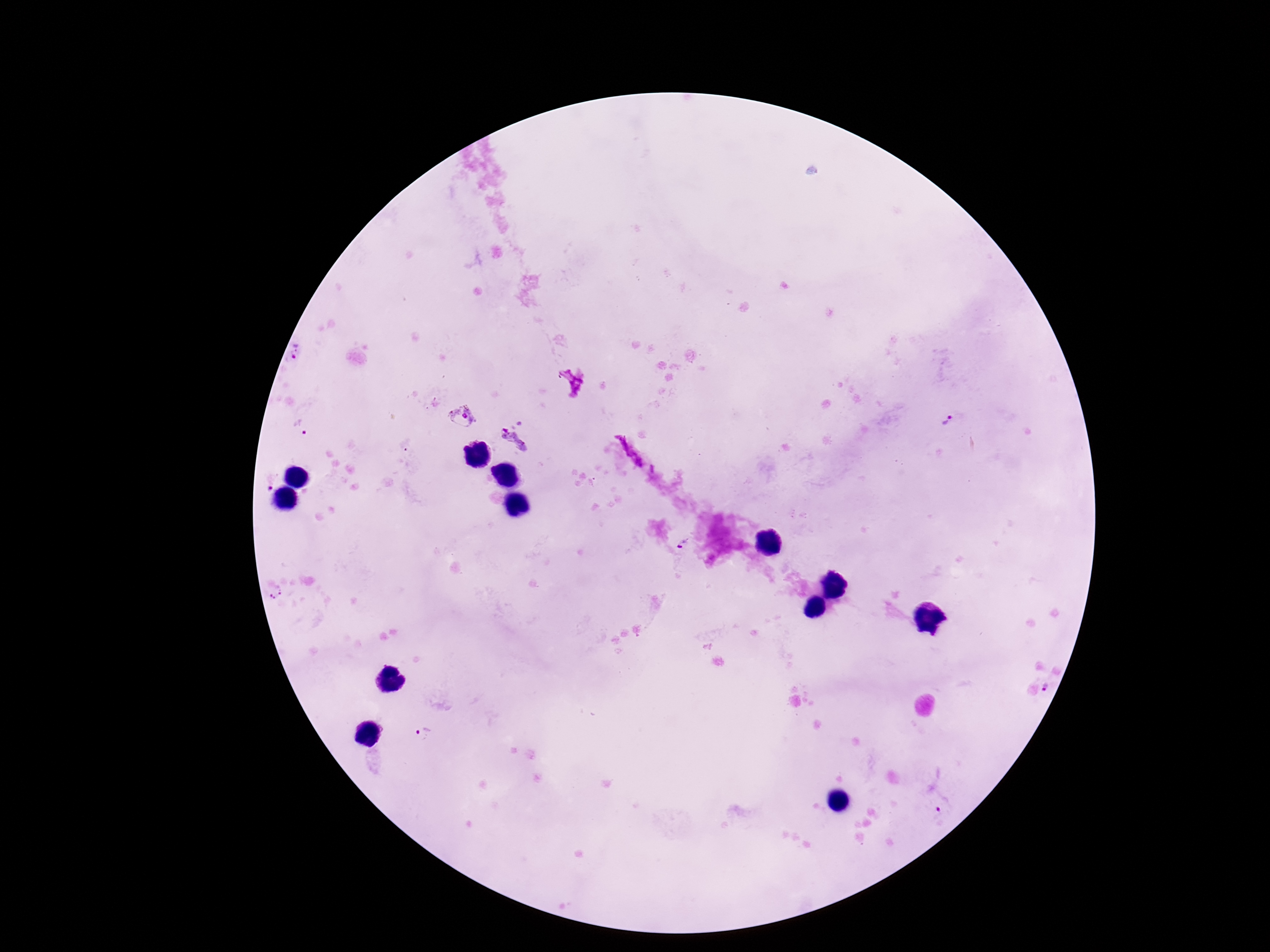

Approximate centers as (x, y) in pixels.
Summary:
  - Plasmodium parasite locations: (297, 354), (463, 418), (948, 421), (300, 430), (515, 439), (269, 481), (684, 545), (276, 593), (1048, 689), (423, 733), (941, 806)
  - Preparation: thick peripheral-blood smear
  - Stain: Giemsa
  - Field of view: single
  - Image size: 1270×952 pixels
  - Patient malaria status: infected
  - Capture: smartphone camera through the microscope eyepiece
  - Magnification: 100x